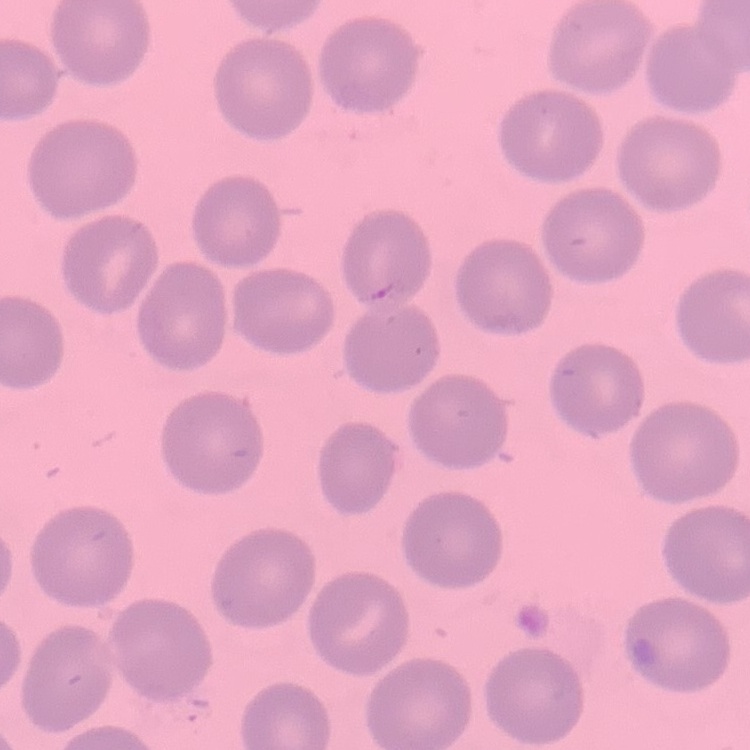 The red blood cells show no rouleaux formation. Thin peripheral smear. Stained with either Field's or Giemsa. Square crop of a larger photomicrograph.